Assess this cell for malaria.
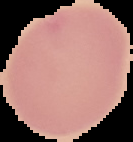

It is uninfected.

From a thin blood smear. Cell region segmented out of the field of view; the surrounding area is masked to black. Image is 133×142 pixels.